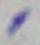

{
  "identification": "Toxoplasma gondii",
  "magnification": "1000x",
  "modality": "micrograph"
}